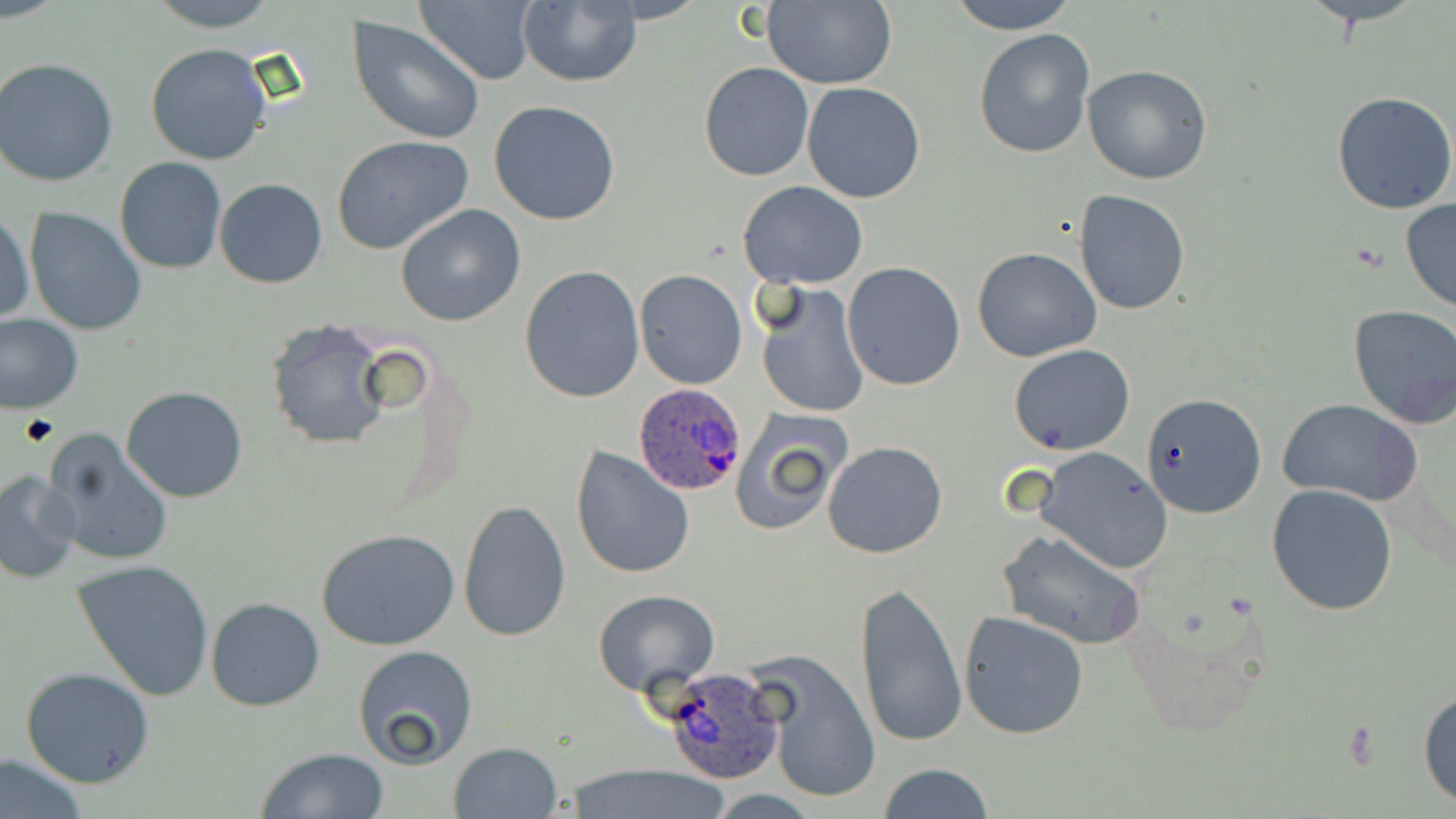
Approximate bounding boxes as (x1,y1)-(x2,y2) corner pairs in pixels. Uninfected red blood cell locations: (144,0)-(284,30), (416,0)-(541,87), (516,0)-(643,88), (760,0)-(897,89), (948,0)-(1077,32), (347,17)-(484,145), (973,27)-(1095,159), (145,43)-(274,166), (0,58)-(120,188), (699,63)-(816,182), (1082,63)-(1212,185), (802,82)-(927,202), (1331,91)-(1456,214), (488,100)-(621,226), (332,135)-(474,255), (114,157)-(227,274), (214,178)-(327,288), (738,181)-(869,289), (1074,190)-(1191,315), (1400,199)-(1456,313), (395,204)-(526,327), (24,207)-(147,336), (0,210)-(34,328), (972,247)-(1101,362), (842,262)-(966,391), (518,264)-(645,403), (634,269)-(747,390), (757,283)-(869,419), (1347,306)-(1456,429), (0,312)-(83,413), (265,317)-(392,451), (1010,345)-(1134,455), (120,385)-(249,503), (1140,391)-(1266,520), (1277,397)-(1424,506), (729,406)-(852,537), (40,428)-(176,568), (822,442)-(948,558), (569,445)-(695,580), (1032,447)-(1177,575), (0,471)-(83,583), (1266,483)-(1399,615), (458,498)-(572,643), (316,528)-(461,651), (997,529)-(1147,649), (72,558)-(215,701), (855,577)-(966,751), (592,588)-(720,696), (206,596)-(325,711), (1121,597)-(1275,743), (959,610)-(1091,740), (352,645)-(478,770), (751,650)-(882,805), (21,668)-(154,788), (1418,687)-(1456,810), (448,742)-(562,818), (255,746)-(390,819), (0,754)-(88,818), (876,763)-(995,819), (565,764)-(729,818). Platelet locations: (21,414)-(60,446). Plasmodium ovale-infected red blood cell locations: (632,383)-(745,498), (659,661)-(785,786). Slide-level diagnosis: Plasmodium ovale. Image is 1456×819 pixels. Captured at 1000x magnification. Single field of view. Thin blood smear. May-Grünwald-Giemsa stain. Optical microscopy.